Locate every blood parasite and identify its species.
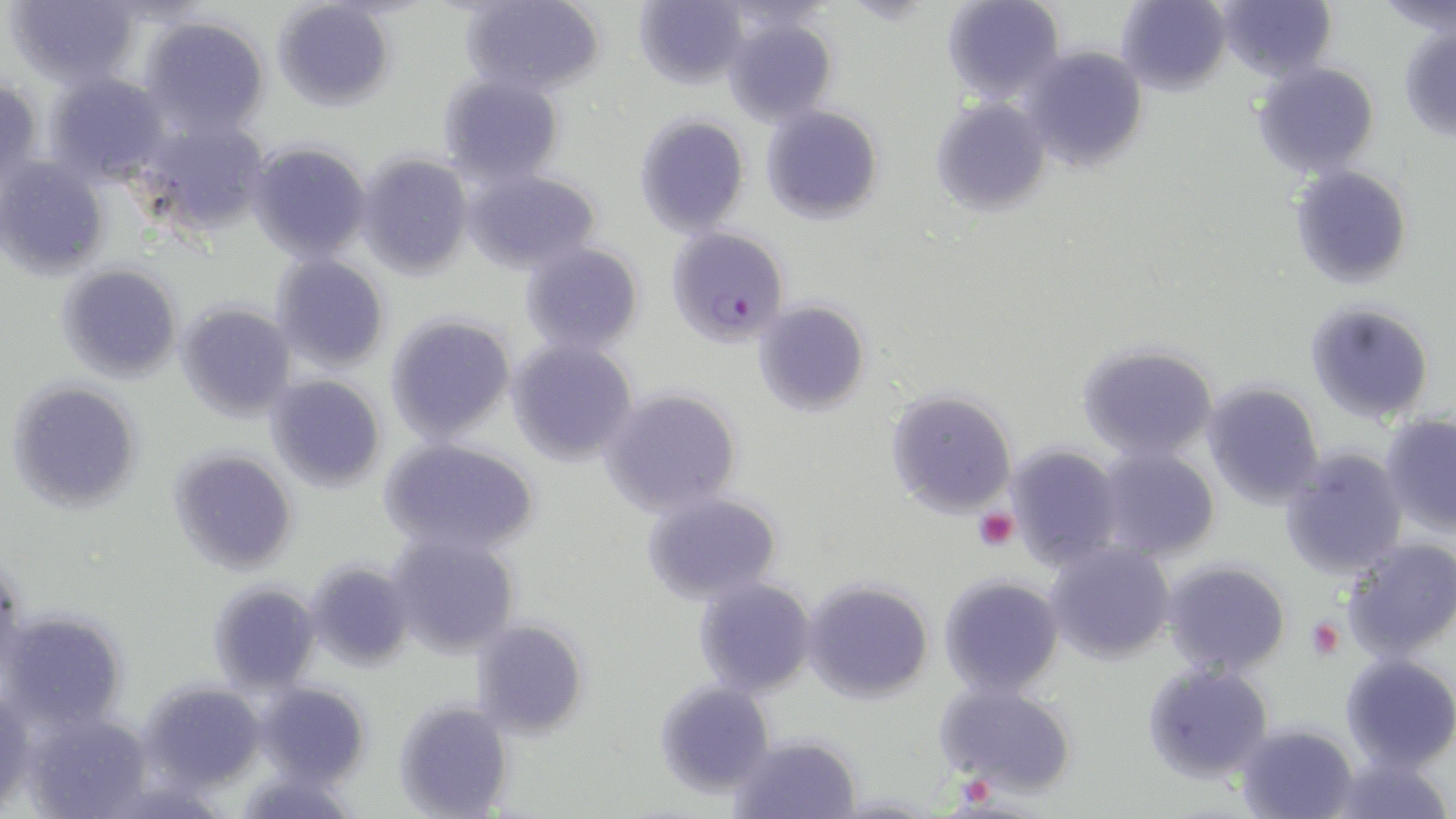

Approximate bounding boxes as (x1,y1)-(x2,y2) corner pairs in pixels.
Plasmodium falciparum-infected red blood cells: (665,229)-(787,347).
No Plasmodium ovale, Plasmodium malariae, Plasmodium vivax, Babesia divergens, or Trypanosoma brucei observed.

Platelet locations: (974,509)-(1019,552), (1305,618)-(1345,660). Uninfected red blood cell locations: (6,0)-(143,88), (462,0)-(605,98), (632,0)-(750,88), (941,0)-(1064,103), (1117,0)-(1233,93), (1215,0)-(1336,82), (1378,0)-(1456,39), (272,1)-(398,109), (723,12)-(837,124), (137,14)-(270,140), (1398,23)-(1456,140), (1018,45)-(1148,171), (1251,62)-(1382,179), (43,71)-(170,182), (438,73)-(564,183), (0,74)-(45,193), (931,97)-(1052,217), (761,105)-(883,224), (632,113)-(751,236), (136,114)-(271,235), (246,140)-(373,264), (356,152)-(473,278), (0,156)-(108,278), (1289,164)-(1412,288), (464,169)-(601,272), (520,242)-(647,356), (270,253)-(390,372), (58,263)-(181,383), (176,300)-(297,421), (754,300)-(871,417), (1304,300)-(1435,426), (384,313)-(516,443), (505,339)-(638,467), (1077,342)-(1219,464), (265,375)-(388,493), (1200,380)-(1326,508), (8,381)-(142,514), (600,387)-(744,518), (884,387)-(1020,520), (1380,412)-(1456,535), (378,439)-(540,559), (1003,441)-(1126,570), (1277,446)-(1408,582), (171,447)-(298,574), (1092,447)-(1221,562), (642,493)-(783,603), (386,532)-(520,658), (1340,539)-(1456,663), (1046,541)-(1175,664), (1162,559)-(1290,678), (305,561)-(414,669), (938,574)-(1064,698), (693,579)-(816,697), (801,579)-(933,701), (210,582)-(321,692), (4,610)-(129,732), (471,617)-(589,740), (1340,652)-(1456,772), (1140,662)-(1275,784), (139,679)-(268,794), (934,680)-(1080,797), (253,681)-(373,789), (655,681)-(776,797), (1,684)-(34,815), (395,698)-(514,817), (21,709)-(154,819), (1234,720)-(1361,819), (727,734)-(863,819), (1321,750)-(1456,819). Slide-level diagnosis: Plasmodium falciparum. Thin blood smear. 1000x magnification. May-Grünwald-Giemsa-stained preparation. Image is 1456×819 pixels. Light microscopy. Single field of view.